Outline each blood parasite and name the species.
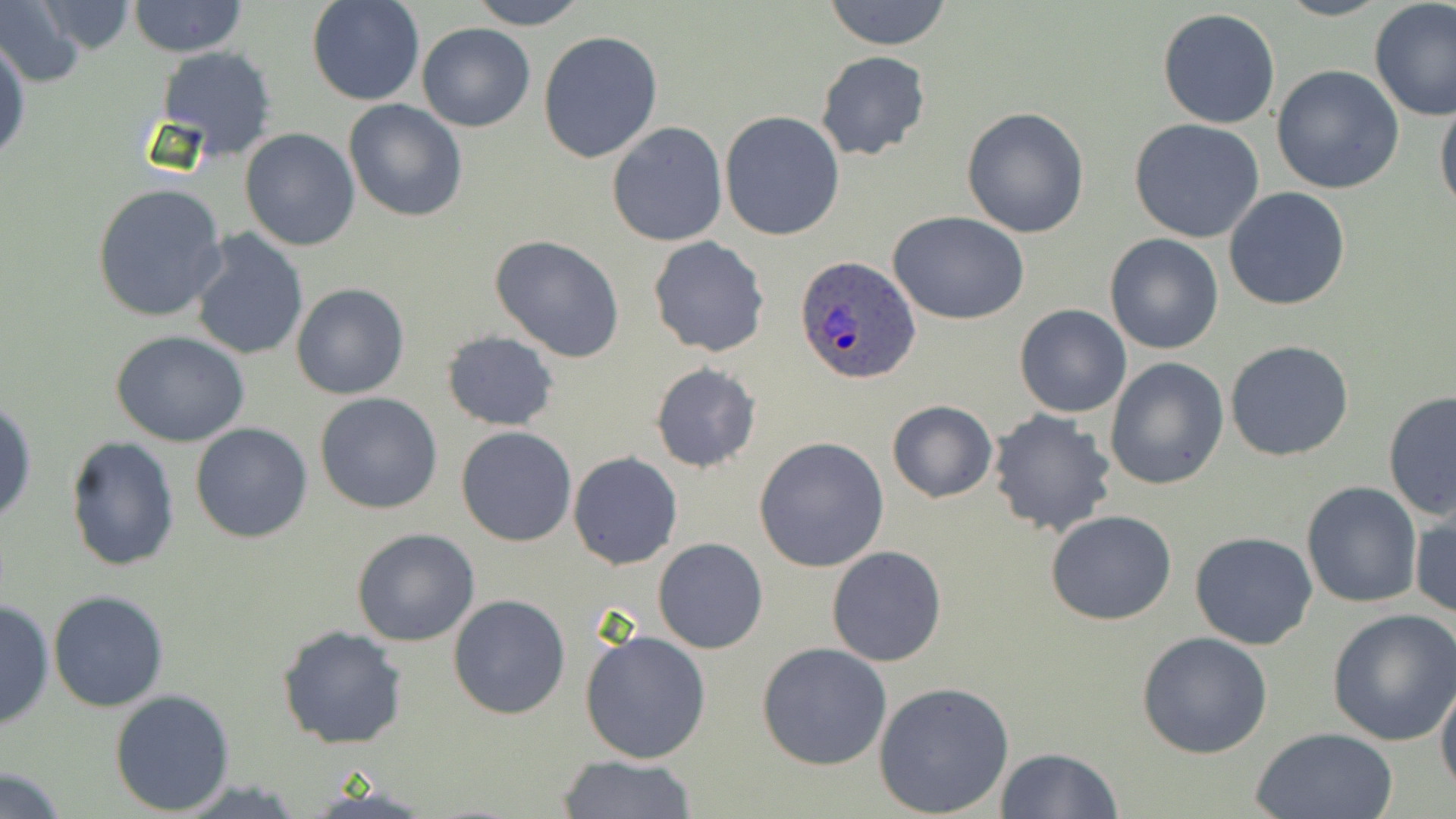
Approximate bounding boxes as (x1, y1, x2, y2) in pixels.
Plasmodium ovale-infected red blood cells: (794, 255, 922, 386).
No Plasmodium falciparum, Plasmodium malariae, Plasmodium vivax, Babesia divergens, or Trypanosoma brucei observed.

slide_level_diagnosis: Plasmodium ovale
field_of_view: single
preparation: thin blood smear
modality: light microscopy
magnification: 1000x
image_size: 1456×819 pixels
stain: May-Grünwald-Giemsa
uninfected_red_blood_cell_locations: 'approximate bounding boxes as (x1, y1, x2, y2) in pixels: (0, 0, 88, 89), (306, 0, 425, 107), (469, 0, 586, 29), (822, 0, 953, 51), (1368, 0, 1456, 120), (26, 1, 144, 58), (127, 1, 247, 58), (1157, 8, 1282, 129), (418, 23, 535, 132), (537, 30, 664, 163), (1, 33, 29, 166), (154, 46, 279, 161), (816, 50, 931, 161), (1270, 65, 1404, 194), (1434, 97, 1455, 220), (343, 100, 470, 222), (961, 105, 1091, 240), (719, 111, 846, 242), (1129, 118, 1267, 244), (607, 122, 728, 247), (240, 127, 361, 250), (92, 182, 229, 324), (1223, 188, 1352, 311), (890, 212, 1029, 325), (187, 231, 309, 360), (1103, 233, 1225, 355), (491, 234, 625, 361), (647, 238, 770, 357), (291, 283, 409, 400), (1014, 304, 1132, 418), (110, 330, 252, 446), (440, 330, 561, 431), (1225, 341, 1354, 462), (1104, 357, 1229, 489), (649, 361, 763, 474), (1381, 389, 1456, 523), (315, 392, 444, 514), (1, 398, 37, 526), (886, 400, 997, 503), (987, 409, 1119, 539), (189, 422, 313, 544), (456, 427, 577, 547), (63, 436, 181, 574), (754, 436, 890, 573), (568, 451, 683, 570), (1301, 480, 1422, 609), (1411, 505, 1455, 622), (1045, 510, 1176, 626), (351, 528, 479, 647), (1190, 531, 1317, 649), (653, 538, 768, 654), (826, 546, 947, 666), (48, 589, 170, 712), (447, 594, 570, 720), (0, 597, 54, 732), (1327, 608, 1456, 745), (278, 625, 407, 750), (579, 627, 711, 764), (1136, 632, 1274, 758), (757, 642, 891, 771), (1435, 674, 1456, 797), (874, 680, 1014, 817), (109, 688, 236, 813), (1251, 727, 1399, 818), (993, 747, 1123, 818), (557, 755, 700, 817), (0, 766, 70, 819)'